Assess this cell for malaria.
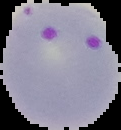
Parasitized.

From a thin blood film. Segmented cell region on a black background. Image is 121×130 pixels.